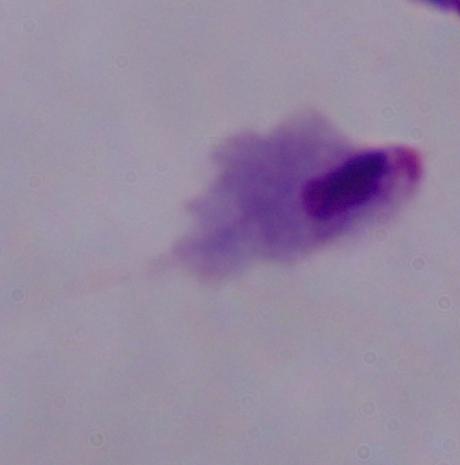
modality: photomicrograph
magnification: 1000x
identification: trichomonad